Outline each blood parasite and name the species.
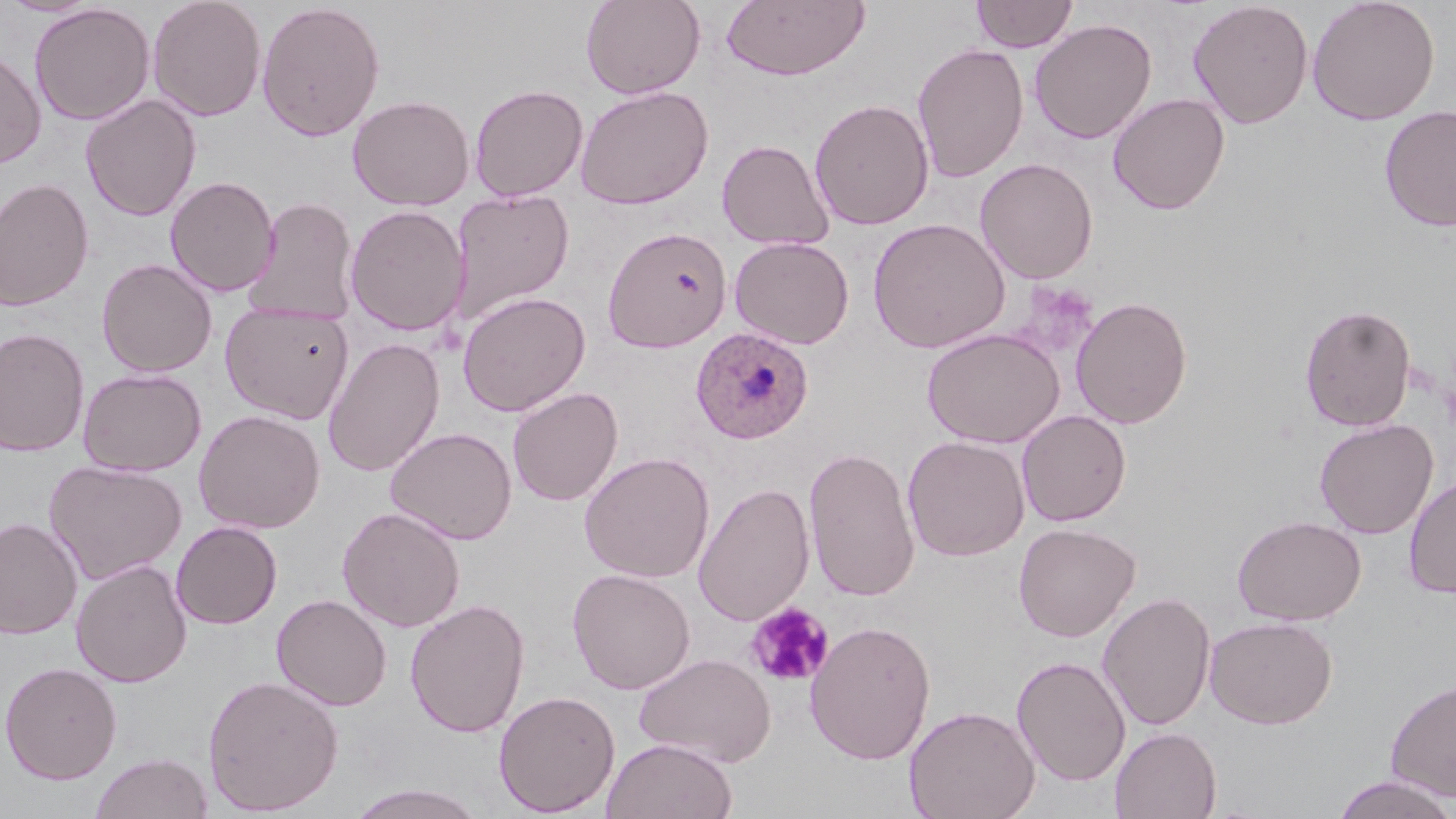
Approximate bounding boxes as named x1/y1/x2/y2 corners in pixels.
Plasmodium ovale-infected red blood cells: (x1=690, y1=327, x2=814, y2=444).
No Plasmodium falciparum, Plasmodium malariae, Plasmodium vivax, Babesia divergens, or Trypanosoma brucei observed.

Uninfected red blood cell locations: (x1=0, y1=0, x2=105, y2=17), (x1=147, y1=0, x2=267, y2=122), (x1=580, y1=0, x2=705, y2=99), (x1=720, y1=0, x2=870, y2=81), (x1=971, y1=0, x2=1078, y2=53), (x1=1187, y1=0, x2=1314, y2=129), (x1=1307, y1=0, x2=1440, y2=126), (x1=256, y1=2, x2=386, y2=142), (x1=29, y1=3, x2=155, y2=126), (x1=1030, y1=18, x2=1157, y2=144), (x1=912, y1=43, x2=1029, y2=183), (x1=0, y1=48, x2=47, y2=171), (x1=469, y1=83, x2=588, y2=202), (x1=575, y1=85, x2=713, y2=210), (x1=1108, y1=92, x2=1230, y2=214), (x1=80, y1=94, x2=202, y2=221), (x1=348, y1=94, x2=474, y2=211), (x1=809, y1=98, x2=934, y2=231), (x1=1379, y1=105, x2=1456, y2=232), (x1=716, y1=139, x2=835, y2=251), (x1=975, y1=158, x2=1098, y2=283), (x1=165, y1=176, x2=280, y2=297), (x1=0, y1=177, x2=95, y2=312), (x1=451, y1=189, x2=575, y2=324), (x1=246, y1=197, x2=359, y2=325), (x1=344, y1=205, x2=469, y2=336), (x1=868, y1=217, x2=1011, y2=354), (x1=602, y1=226, x2=732, y2=352), (x1=729, y1=236, x2=854, y2=349), (x1=96, y1=258, x2=217, y2=378), (x1=457, y1=291, x2=590, y2=417), (x1=1070, y1=296, x2=1193, y2=429), (x1=220, y1=301, x2=354, y2=423), (x1=1299, y1=303, x2=1417, y2=432), (x1=921, y1=327, x2=1065, y2=448), (x1=0, y1=328, x2=90, y2=457), (x1=323, y1=338, x2=445, y2=477), (x1=77, y1=368, x2=207, y2=477), (x1=507, y1=386, x2=623, y2=506), (x1=193, y1=409, x2=326, y2=534), (x1=1016, y1=409, x2=1131, y2=526), (x1=1314, y1=418, x2=1438, y2=540), (x1=385, y1=427, x2=517, y2=544), (x1=902, y1=435, x2=1030, y2=561), (x1=803, y1=446, x2=921, y2=602), (x1=579, y1=452, x2=715, y2=583), (x1=44, y1=460, x2=187, y2=585), (x1=1403, y1=475, x2=1456, y2=598), (x1=694, y1=482, x2=815, y2=626), (x1=336, y1=506, x2=466, y2=632), (x1=1233, y1=514, x2=1367, y2=626), (x1=0, y1=517, x2=82, y2=640), (x1=170, y1=520, x2=282, y2=629), (x1=1013, y1=522, x2=1140, y2=641), (x1=70, y1=559, x2=192, y2=688), (x1=567, y1=568, x2=695, y2=694), (x1=1097, y1=591, x2=1216, y2=732), (x1=271, y1=593, x2=392, y2=711), (x1=405, y1=598, x2=530, y2=738), (x1=1204, y1=615, x2=1338, y2=729), (x1=804, y1=620, x2=937, y2=764), (x1=634, y1=652, x2=775, y2=767), (x1=1011, y1=655, x2=1131, y2=787), (x1=0, y1=661, x2=122, y2=784), (x1=202, y1=674, x2=344, y2=815), (x1=1385, y1=678, x2=1456, y2=802), (x1=493, y1=689, x2=620, y2=817), (x1=904, y1=704, x2=1040, y2=819), (x1=1110, y1=726, x2=1221, y2=819), (x1=601, y1=737, x2=738, y2=819), (x1=89, y1=751, x2=213, y2=818), (x1=1331, y1=775, x2=1455, y2=819), (x1=346, y1=783, x2=490, y2=819). Platelet locations: (x1=746, y1=601, x2=835, y2=689). Slide-level diagnosis: Plasmodium ovale. Captured at 1000x magnification. Single field of view. May-Grünwald-Giemsa stain. Thin blood smear. Image is 1456×819 pixels. Light microscopy.